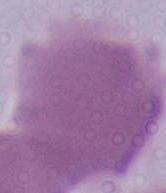

magnification = 1000x
identification = red blood cell
modality = micrograph